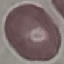

Result: no malaria parasites seen. Acquired by smartphone through the microscope eyepiece. Giemsa stain. Cell patch, automatically extracted from a larger field of view and resized to 64 × 64 pixels. Thin blood smear.